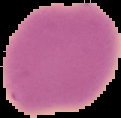
image type = cell region segmented out of the field of view; surrounding area masked to black
image size = 121×118 pixels
preparation = thin blood film
malaria status = uninfected